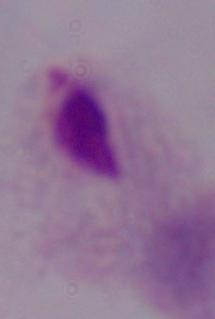

Summary:
  - Identification: trichomonad
  - Magnification: 1000x
  - Modality: photomicrograph